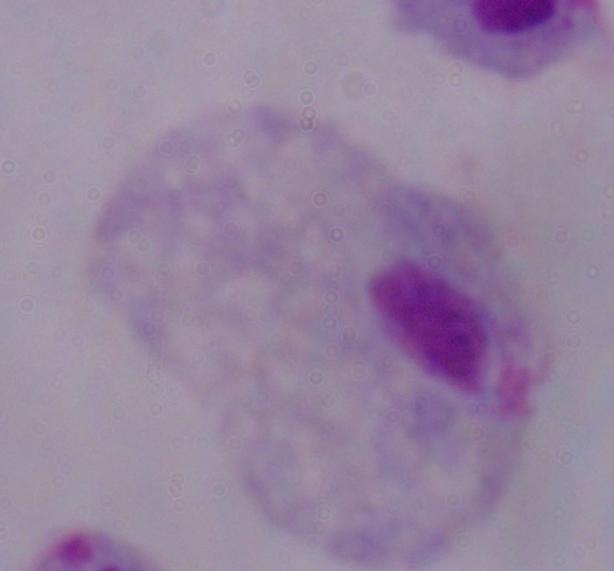 A trichomonad is seen. Photomicrograph. 1000x magnification.